Classify this cell by malaria status.
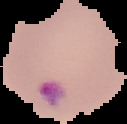
Parasitized.

Summary:
  - Image type: segmented cell region on a black background
  - Preparation: thin blood film
  - Image size: 127×124 pixels